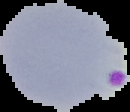

Summary:
  - Malaria status: parasitized
  - Image type: segmented cell region on a black background
  - Image size: 130×112 pixels
  - Preparation: thin blood smear